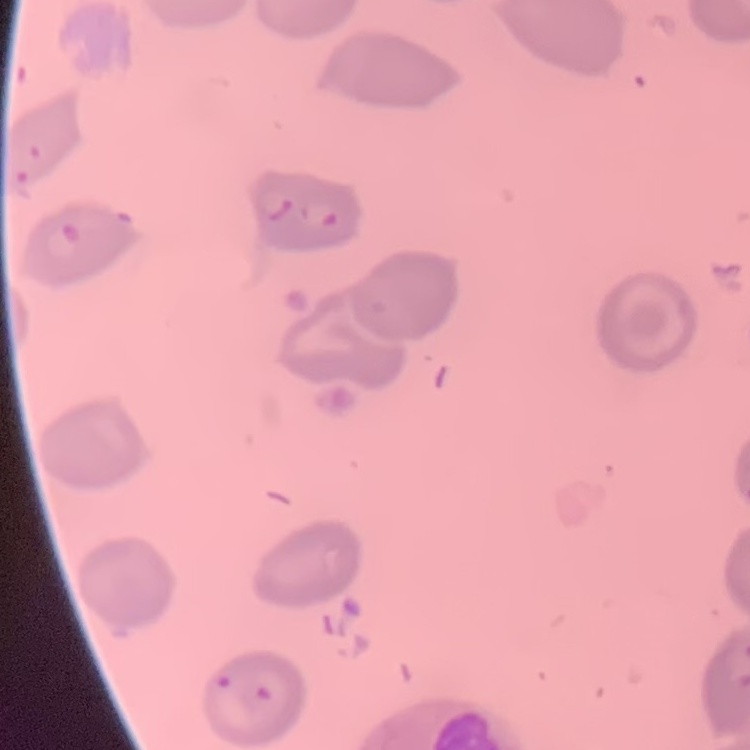 The erythrocytes show no rouleaux formation. Thin blood film. One tile cut from a larger photomicrograph. Stained with either Field's or Giemsa.